Assess the morphology of the red blood cells.
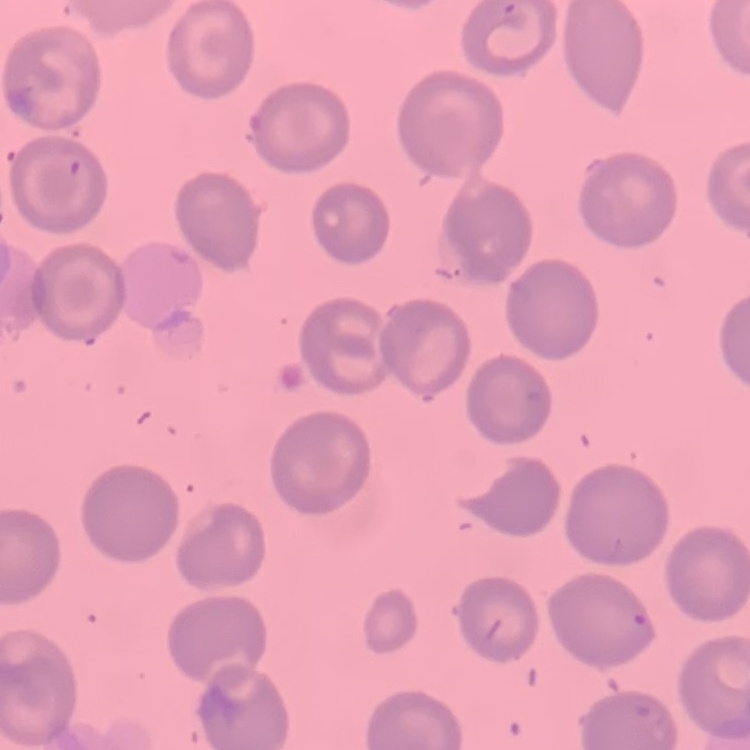

No rouleaux formation.

Summary:
  - Preparation: thin blood smear
  - Image type: one tile cut from a larger photomicrograph
  - Stain: Field's or Giemsa